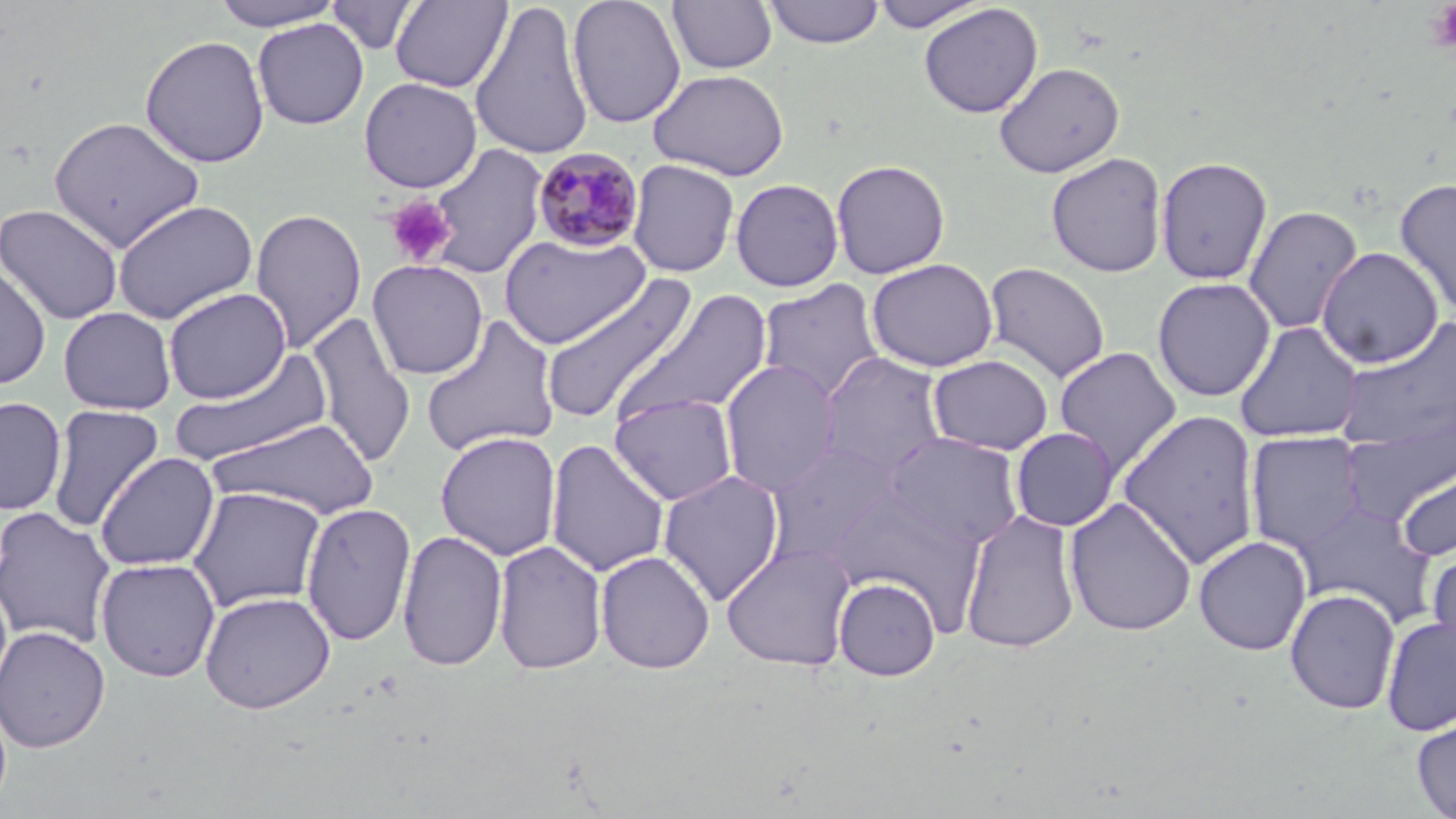

Summary:
  - Coordinate format: approximate bounding boxes as named x1/y1/x2/y2 corners in pixels
  - Uninfected red blood cell locations: (x1=209, y1=0, x2=347, y2=30), (x1=326, y1=0, x2=420, y2=56), (x1=567, y1=0, x2=686, y2=128), (x1=666, y1=0, x2=779, y2=74), (x1=870, y1=0, x2=989, y2=32), (x1=390, y1=1, x2=512, y2=92), (x1=469, y1=1, x2=595, y2=161), (x1=763, y1=1, x2=886, y2=48), (x1=918, y1=3, x2=1043, y2=119), (x1=252, y1=18, x2=369, y2=129), (x1=140, y1=34, x2=270, y2=168), (x1=994, y1=62, x2=1125, y2=178), (x1=649, y1=68, x2=790, y2=181), (x1=358, y1=76, x2=482, y2=193), (x1=48, y1=115, x2=205, y2=253), (x1=424, y1=143, x2=549, y2=280), (x1=1046, y1=152, x2=1167, y2=278), (x1=1155, y1=156, x2=1273, y2=285), (x1=627, y1=159, x2=740, y2=278), (x1=830, y1=159, x2=951, y2=279), (x1=730, y1=178, x2=844, y2=292), (x1=1394, y1=178, x2=1456, y2=316), (x1=111, y1=200, x2=259, y2=325), (x1=0, y1=203, x2=124, y2=325), (x1=1243, y1=205, x2=1363, y2=335), (x1=251, y1=208, x2=367, y2=353), (x1=498, y1=232, x2=651, y2=350), (x1=1316, y1=246, x2=1443, y2=369), (x1=866, y1=258, x2=998, y2=373), (x1=367, y1=259, x2=489, y2=380), (x1=983, y1=261, x2=1110, y2=384), (x1=0, y1=262, x2=52, y2=389), (x1=538, y1=273, x2=697, y2=425), (x1=1152, y1=277, x2=1276, y2=402), (x1=757, y1=279, x2=887, y2=404), (x1=163, y1=287, x2=291, y2=404), (x1=616, y1=289, x2=773, y2=427), (x1=58, y1=306, x2=176, y2=414), (x1=306, y1=312, x2=416, y2=468), (x1=421, y1=316, x2=560, y2=458), (x1=1336, y1=316, x2=1456, y2=453), (x1=1234, y1=321, x2=1364, y2=443), (x1=1053, y1=346, x2=1182, y2=478), (x1=169, y1=347, x2=336, y2=467), (x1=817, y1=352, x2=950, y2=479), (x1=927, y1=354, x2=1054, y2=456), (x1=719, y1=360, x2=840, y2=496), (x1=609, y1=393, x2=738, y2=506), (x1=0, y1=396, x2=67, y2=516), (x1=47, y1=404, x2=165, y2=532), (x1=1117, y1=409, x2=1262, y2=569), (x1=1342, y1=413, x2=1456, y2=529), (x1=208, y1=417, x2=380, y2=520), (x1=1010, y1=427, x2=1120, y2=531), (x1=434, y1=431, x2=562, y2=561), (x1=1245, y1=431, x2=1367, y2=553), (x1=883, y1=432, x2=1024, y2=550), (x1=544, y1=438, x2=670, y2=577), (x1=763, y1=442, x2=900, y2=567), (x1=94, y1=452, x2=220, y2=571), (x1=1396, y1=456, x2=1456, y2=564), (x1=657, y1=469, x2=785, y2=606), (x1=186, y1=486, x2=327, y2=613), (x1=832, y1=490, x2=984, y2=626), (x1=1063, y1=497, x2=1198, y2=637), (x1=1292, y1=499, x2=1437, y2=626), (x1=300, y1=502, x2=416, y2=646), (x1=0, y1=507, x2=118, y2=650), (x1=959, y1=508, x2=1081, y2=653), (x1=397, y1=528, x2=508, y2=672), (x1=1193, y1=535, x2=1312, y2=656), (x1=492, y1=539, x2=608, y2=675), (x1=721, y1=543, x2=856, y2=670), (x1=1427, y1=546, x2=1456, y2=663), (x1=594, y1=550, x2=715, y2=674), (x1=95, y1=557, x2=221, y2=682), (x1=833, y1=576, x2=941, y2=681), (x1=1284, y1=588, x2=1400, y2=714), (x1=199, y1=590, x2=336, y2=713), (x1=1380, y1=615, x2=1456, y2=737), (x1=0, y1=625, x2=111, y2=753), (x1=1411, y1=711, x2=1456, y2=819)
  - Plasmodium malariae-infected red blood cell locations: (x1=531, y1=147, x2=646, y2=253)
  - Platelet locations: (x1=1425, y1=2, x2=1456, y2=53), (x1=384, y1=195, x2=456, y2=267)
  - Slide-level diagnosis: Plasmodium malariae
  - Preparation: thin blood film
  - Magnification: 1000x
  - Modality: optical microscopy
  - Image size: 1456×819 pixels
  - Stain: May-Grünwald-Giemsa
  - Field of view: one of a larger specimen